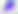
magnification = 400x
identification = Toxoplasma gondii
modality = micrograph